Outline each Plasmodium vivax-infected red blood cell.
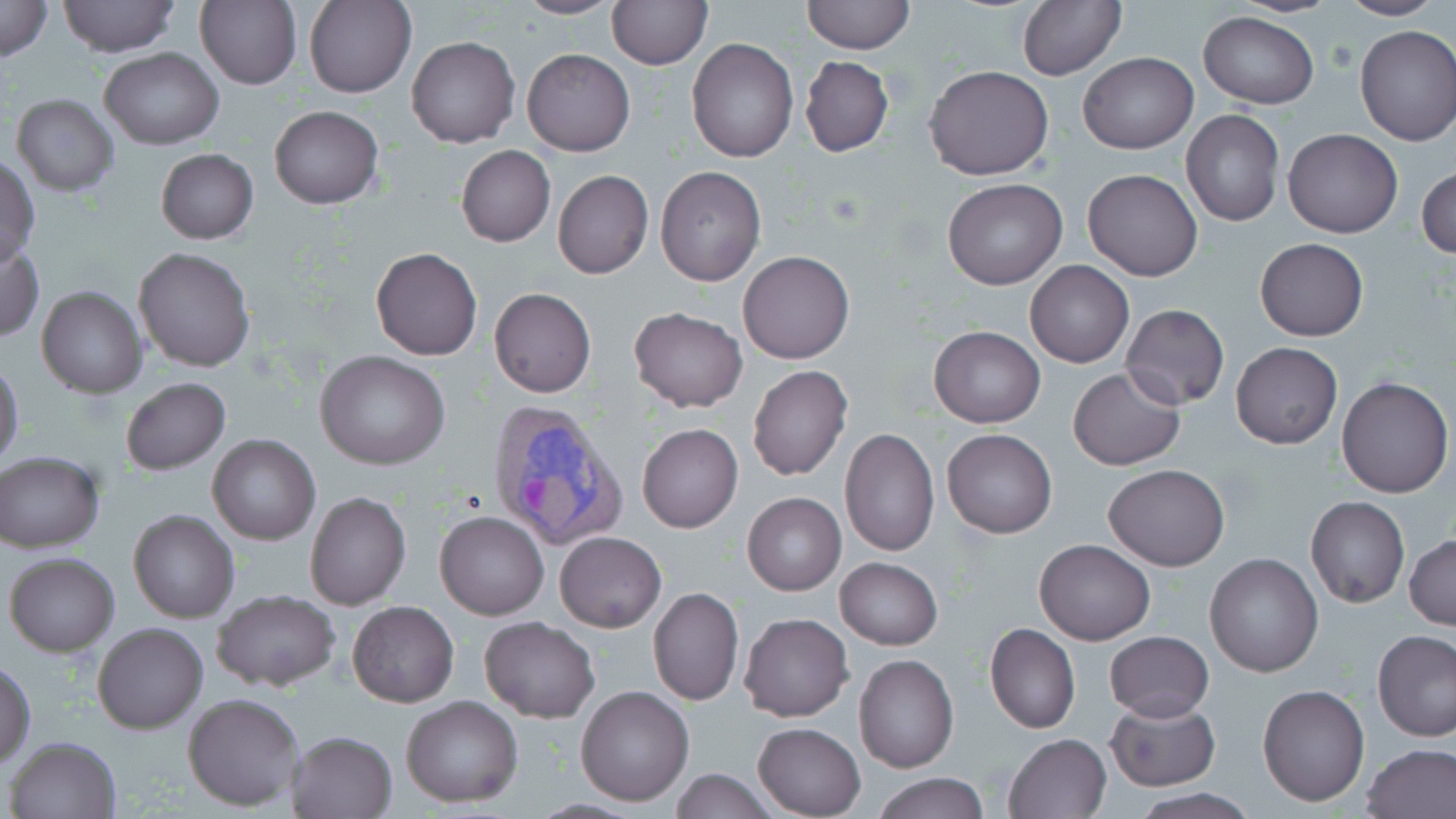
Approximate bounding boxes as (x1, y1, x2, y2) in pixels.
Plasmodium vivax-infected red blood cells: (486, 399, 627, 552).

Summary:
  - Uninfected red blood cell locations: (0, 0, 52, 62), (56, 0, 179, 58), (196, 0, 303, 91), (304, 0, 415, 99), (513, 0, 622, 19), (607, 0, 710, 68), (801, 0, 915, 54), (1017, 0, 1124, 81), (1336, 0, 1445, 22), (1199, 11, 1319, 110), (1355, 24, 1456, 148), (406, 35, 521, 149), (685, 38, 799, 163), (100, 47, 224, 150), (522, 48, 634, 156), (1078, 53, 1198, 153), (799, 57, 894, 157), (926, 65, 1054, 181), (12, 94, 119, 196), (269, 107, 384, 209), (1181, 109, 1284, 226), (1282, 129, 1402, 238), (456, 145, 555, 247), (156, 148, 257, 245), (0, 156, 39, 266), (1418, 165, 1456, 261), (655, 167, 766, 286), (1082, 169, 1202, 281), (553, 170, 654, 279), (942, 178, 1066, 290), (1255, 238, 1368, 341), (0, 239, 43, 340), (132, 246, 256, 372), (370, 247, 481, 360), (738, 249, 856, 364), (1024, 261, 1134, 368), (37, 285, 146, 398), (489, 288, 596, 398), (1121, 304, 1230, 409), (628, 306, 748, 413), (928, 325, 1045, 429), (1231, 342, 1342, 448), (314, 350, 450, 469), (0, 361, 23, 467), (748, 364, 853, 481), (1068, 367, 1186, 471), (1336, 377, 1452, 498), (122, 378, 230, 476), (637, 423, 744, 533), (839, 427, 940, 558), (943, 428, 1056, 537), (206, 432, 321, 546), (0, 451, 105, 552), (1104, 464, 1229, 571), (306, 491, 411, 610), (743, 493, 846, 595), (1306, 497, 1410, 609), (129, 509, 238, 623), (435, 510, 549, 620), (555, 532, 666, 632), (1406, 534, 1455, 629), (1035, 538, 1155, 645), (4, 551, 119, 656), (1205, 553, 1324, 676), (835, 558, 943, 650), (649, 587, 744, 707), (210, 589, 340, 691), (348, 601, 457, 708), (739, 612, 854, 723), (480, 615, 599, 722), (93, 621, 208, 735), (984, 623, 1080, 734), (1373, 631, 1456, 742), (1105, 632, 1213, 720), (853, 653, 958, 773), (1, 662, 36, 764), (1258, 682, 1371, 807), (575, 686, 693, 805), (183, 692, 306, 809), (400, 695, 524, 807), (1103, 698, 1220, 791), (751, 721, 867, 818), (287, 729, 398, 818), (1003, 732, 1111, 819), (4, 736, 123, 819), (1362, 743, 1456, 819), (668, 768, 779, 819), (872, 774, 988, 818), (1128, 789, 1260, 819)
  - Slide-level diagnosis: Plasmodium vivax
  - Image size: 1456×819 pixels
  - Preparation: thin blood film
  - Magnification: 1000x
  - Stain: May-Grünwald-Giemsa
  - Modality: optical microscopy
  - Field of view: single